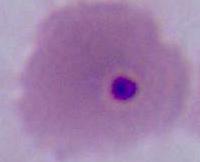

Summary:
  - Modality: micrograph
  - Magnification: 400x or 1000x
  - Identification: Plasmodium